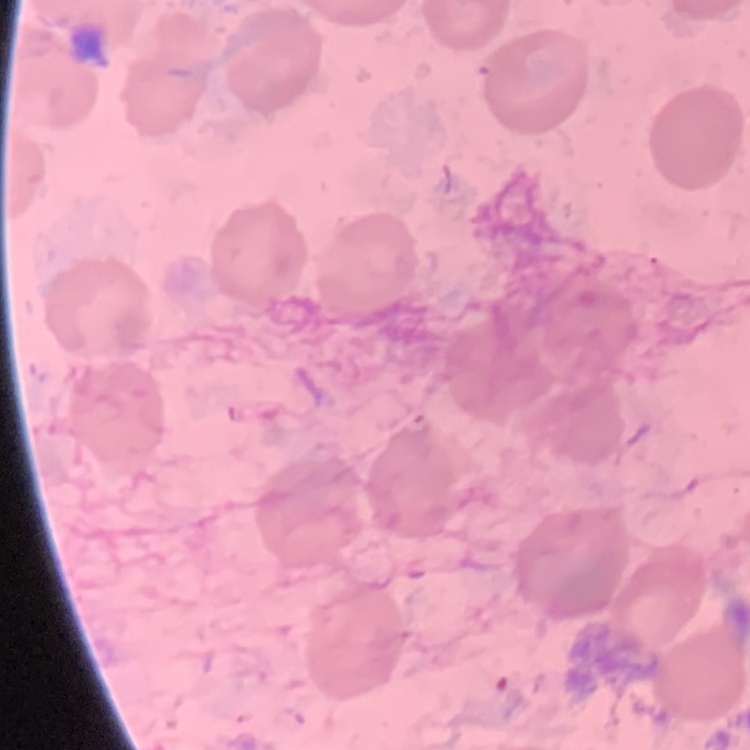

red blood cell morphology = no rouleaux formation
preparation = thin peripheral smear
stain = Field's or Giemsa
image type = square crop of a larger photomicrograph